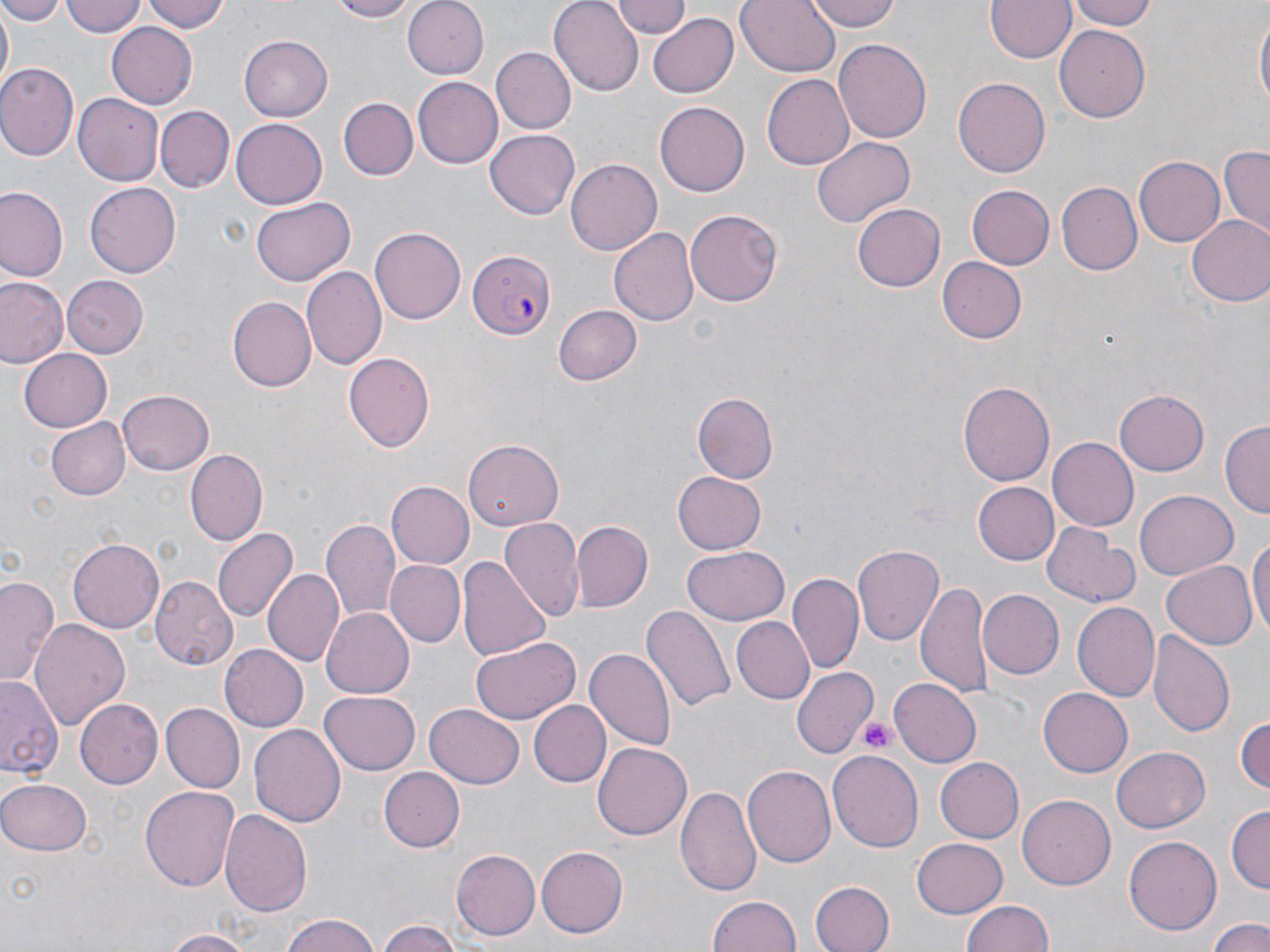

{
  "slide_level_diagnosis": "Plasmodium falciparum",
  "preparation": "thin blood smear",
  "platelet_locations": "approximate bounding boxes as (x1,y1)-(x2,y2) corner pairs in pixels: (858,715)-(899,755)",
  "magnification": "1000x",
  "uninfected_red_blood_cell_locations": "approximate bounding boxes as (x1,y1)-(x2,y2) corner pairs in pixels: (0,0)-(65,24), (61,0)-(146,40), (142,0)-(226,33), (323,0)-(423,22), (405,0)-(488,80), (550,0)-(641,91), (613,0)-(691,38), (736,0)-(840,77), (806,0)-(901,31), (987,0)-(1075,63), (1067,0)-(1157,31), (1,8)-(12,88), (1254,8)-(1269,118), (646,12)-(738,97), (105,21)-(197,108), (1055,26)-(1150,122), (238,35)-(333,120), (833,39)-(931,146), (489,47)-(575,135), (0,63)-(78,160), (762,73)-(855,170), (412,77)-(502,168), (953,77)-(1051,177), (73,92)-(163,186), (339,98)-(418,181), (654,102)-(750,197), (157,107)-(233,193), (232,120)-(326,208), (485,128)-(579,216), (812,136)-(915,228), (1219,146)-(1269,238), (1134,156)-(1226,246), (565,158)-(661,253), (85,182)-(180,279), (1058,182)-(1142,274), (966,185)-(1054,269), (0,187)-(66,282), (251,197)-(356,286), (854,202)-(944,292), (685,208)-(784,305), (1186,215)-(1270,308), (371,226)-(465,324), (611,227)-(699,329), (937,256)-(1026,341), (300,265)-(386,370), (61,275)-(147,359), (1,277)-(67,369), (229,297)-(317,391), (551,304)-(640,386), (17,348)-(112,432), (343,353)-(433,453), (958,380)-(1055,488), (1115,387)-(1209,475), (119,388)-(214,474), (692,392)-(778,483), (44,416)-(130,501), (1221,421)-(1269,520), (1048,437)-(1138,530), (465,440)-(564,530), (187,450)-(266,546), (673,472)-(766,553), (974,481)-(1057,563), (387,482)-(473,568), (1134,490)-(1237,581), (502,518)-(582,621), (322,519)-(400,622), (571,521)-(653,613), (1043,524)-(1139,607), (213,530)-(296,623), (1249,530)-(1270,642), (68,534)-(164,631), (852,544)-(943,648), (681,547)-(790,626), (458,554)-(551,661), (386,561)-(465,647), (1162,561)-(1258,650), (263,569)-(341,665), (790,571)-(862,675), (0,573)-(61,687), (153,575)-(239,672), (917,582)-(993,698), (978,590)-(1063,678), (1072,600)-(1160,701), (644,604)-(734,714), (322,608)-(414,697), (731,616)-(813,704), (29,619)-(128,729), (1149,630)-(1234,735), (470,637)-(580,724), (218,644)-(307,732), (584,646)-(674,748), (792,667)-(877,755), (0,678)-(63,778), (889,678)-(981,766), (1038,689)-(1132,777), (320,692)-(421,774), (74,700)-(162,789), (527,700)-(610,787), (162,703)-(242,791), (425,704)-(523,788), (1235,714)-(1269,798), (248,724)-(344,828), (593,742)-(691,840), (1112,746)-(1211,833), (828,751)-(924,850), (933,757)-(1024,843), (743,766)-(835,869), (378,767)-(463,851), (0,776)-(91,858), (679,784)-(763,898), (139,785)-(241,891), (1018,795)-(1117,889), (1226,806)-(1268,895), (220,808)-(312,918), (1122,836)-(1222,937), (913,837)-(1009,915), (537,847)-(627,938), (452,850)-(540,940), (808,880)-(893,952), (707,894)-(801,952), (960,900)-(1056,952), (279,913)-(383,952), (1207,915)-(1269,951), (376,921)-(466,952), (157,930)-(254,951)",
  "modality": "optical microscopy",
  "plasmodium_falciparum_infected_red_blood_cell_locations": "approximate bounding boxes as (x1,y1)-(x2,y2) corner pairs in pixels: (468,250)-(555,341)",
  "field_of_view": "one of a larger specimen",
  "stain": "May-Grünwald-Giemsa",
  "image_size": "1270×952 pixels"
}